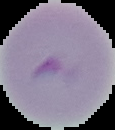

{
  "preparation": "thin blood film",
  "image_size": "115×130 pixels",
  "image_type": "segmented cell region on a black background",
  "malaria_status": "uninfected"
}